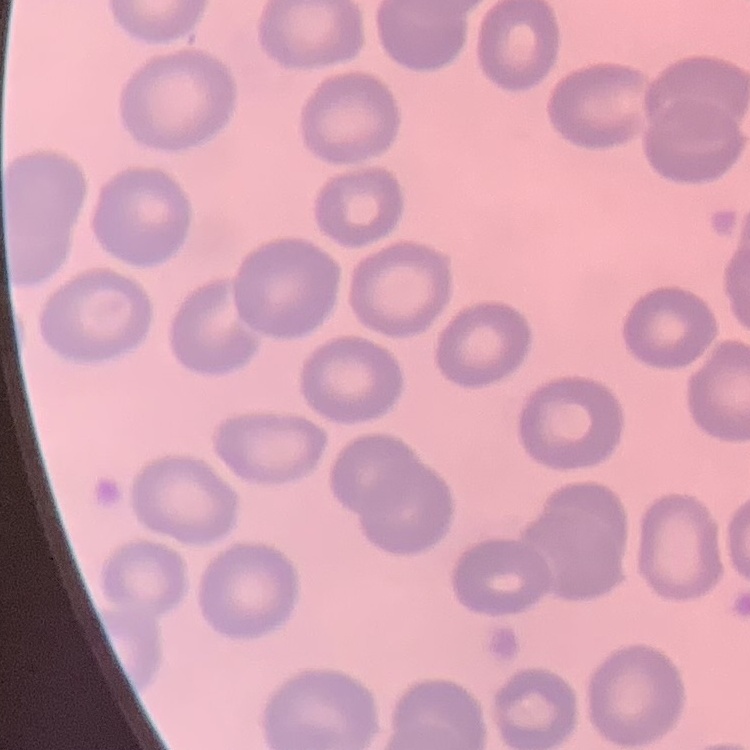

The erythrocytes show no rouleaux formation. Square crop of a larger photomicrograph. Field's or Giemsa stain. Thin blood smear.